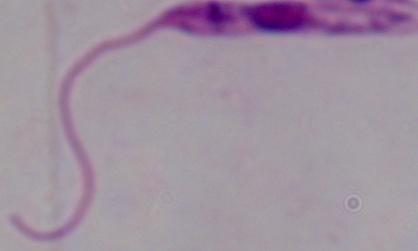
1000x magnification. A Leishmania parasite is shown. Micrograph.